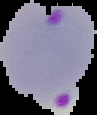
Summary:
  - Malaria status: parasitized
  - Image type: segmented cell region with the area outside set to black
  - Image size: 97×115 pixels
  - Preparation: thin blood smear